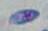
Summary:
  - Identification: Toxoplasma gondii
  - Magnification: 1000x
  - Modality: photomicrograph